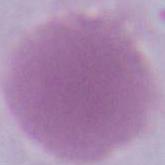
Summary:
  - Magnification: 1000x
  - Identification: erythrocyte
  - Modality: micrograph